Name the parasite shown.
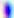

This is Toxoplasma gondii.

Summary:
  - Modality: micrograph
  - Magnification: 400x